Outline each blood parasite and name the species.
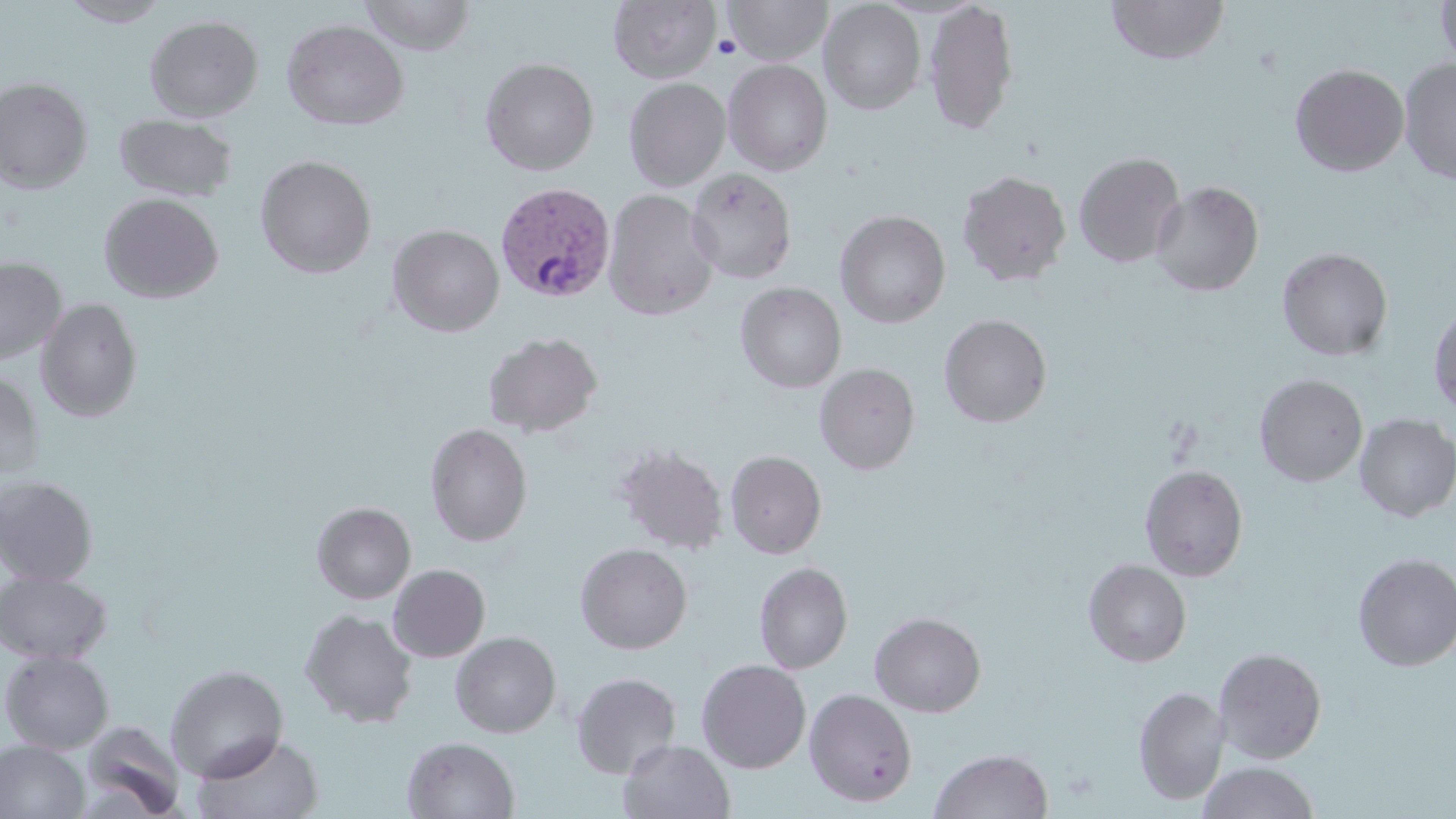

Approximate bounding boxes as [x1, y1, x2, y2] in pixels.
Plasmodium vivax-infected red blood cells: [493, 181, 615, 302].
No Plasmodium falciparum, Plasmodium ovale, Plasmodium malariae, Babesia divergens, or Trypanosoma brucei observed.

slide-level diagnosis = Plasmodium vivax
preparation = thin blood smear
magnification = 1000x
modality = optical microscopy
field of view = single
stain = May-Grünwald-Giemsa
platelet locations = approximate bounding boxes as [x1, y1, x2, y2] in pixels: [713, 34, 742, 59]
image size = 1456×819 pixels
uninfected red blood cell locations = approximate bounding boxes as [x1, y1, x2, y2] in pixels: [359, 0, 476, 55], [608, 0, 720, 84], [722, 0, 833, 65], [924, 0, 1019, 136], [1106, 0, 1231, 65], [1435, 0, 1456, 73], [59, 1, 170, 27], [819, 1, 926, 115], [144, 15, 264, 122], [281, 19, 409, 131], [480, 57, 599, 176], [723, 59, 833, 176], [1399, 59, 1456, 184], [1290, 63, 1409, 177], [0, 77, 94, 194], [623, 77, 730, 191], [114, 113, 238, 202], [1073, 151, 1186, 268], [255, 155, 377, 279], [686, 168, 798, 284], [956, 169, 1072, 287], [1150, 180, 1264, 297], [603, 188, 719, 321], [99, 193, 224, 304], [835, 210, 951, 328], [387, 224, 505, 337], [1276, 247, 1393, 361], [0, 257, 66, 365], [735, 282, 847, 393], [35, 298, 142, 422], [1429, 303, 1456, 419], [938, 314, 1052, 428], [483, 332, 603, 438], [814, 363, 920, 475], [0, 372, 44, 482], [1255, 374, 1368, 486], [1354, 413, 1456, 523], [424, 422, 533, 546], [614, 444, 729, 555], [725, 450, 827, 559], [1139, 464, 1249, 582], [0, 475, 99, 587], [311, 502, 416, 604], [575, 542, 692, 654], [1352, 553, 1456, 671], [1083, 558, 1192, 668], [754, 561, 853, 674], [387, 564, 491, 662], [0, 570, 112, 665], [299, 609, 418, 728], [869, 611, 986, 717], [449, 632, 561, 738], [1214, 647, 1327, 763], [1, 650, 113, 755], [696, 659, 811, 774], [165, 664, 289, 782], [571, 671, 682, 779], [1133, 686, 1230, 805], [804, 688, 918, 807], [78, 721, 186, 819], [192, 733, 324, 819], [402, 735, 520, 819], [617, 738, 736, 819], [0, 741, 89, 819], [928, 747, 1053, 819], [1197, 762, 1321, 819]